Report the malaria status of this cell.
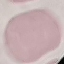
It is uninfected.

Summary:
  - Capture: smartphone camera at the microscope eyepiece
  - Stain: Giemsa
  - Preparation: thin blood film
  - Image type: cell patch, automatically extracted from a larger field of view and resized to 64 × 64 pixels